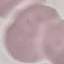

{
  "malaria_status": "uninfected",
  "stain": "Giemsa",
  "image_type": "cell patch, automatically extracted from a larger field of view and resized to 64 × 64 pixels",
  "preparation": "thin smear",
  "capture": "smartphone through the microscope eyepiece"
}